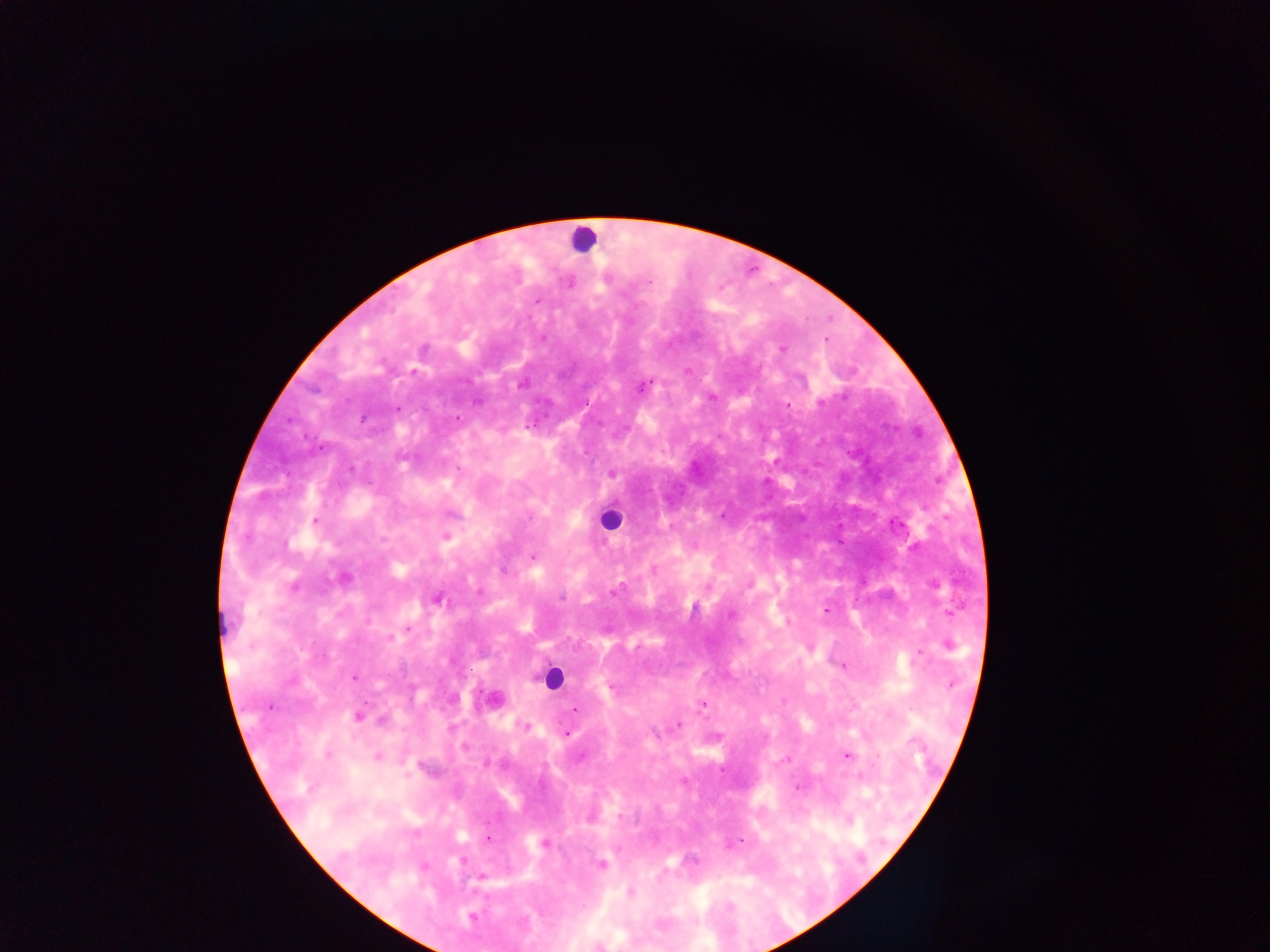

{
  "field_of_view": "single",
  "country": "Ghana",
  "plasmodium_parasite_locations": "approximate centers as {x, y} in pixels: {649, 282}, {537, 300}, {542, 339}, {781, 349}, {413, 371}, {522, 384}, {644, 386}, {712, 398}, {821, 403}, {788, 406}, {398, 408}, {457, 418}, {363, 419}, {527, 426}, {321, 449}, {459, 469}, {611, 474}, {722, 516}, {530, 517}, {315, 521}, {445, 536}, {533, 557}, {344, 578}, {293, 586}, {615, 591}, {562, 597}, {438, 600}, {826, 611}, {730, 616}, {408, 628}, {390, 638}, {949, 646}, {920, 653}, {843, 665}, {353, 677}, {952, 684}, {703, 704}, {270, 706}, {575, 708}, {358, 715}, {525, 726}, {678, 726}, {567, 734}, {464, 747}, {327, 755}, {847, 755}, {378, 756}, {786, 760}, {797, 787}, {488, 839}, {740, 841}, {543, 844}, {601, 865}, {481, 875}, {631, 893}",
  "leukocyte_locations": "approximate centers as {x, y} in pixels: {582, 239}, {611, 518}, {222, 623}, {551, 678}",
  "preparation": "thick blood smear",
  "capture": "mobile-phone photograph through a microscope",
  "image_size": "1270×952 pixels"
}